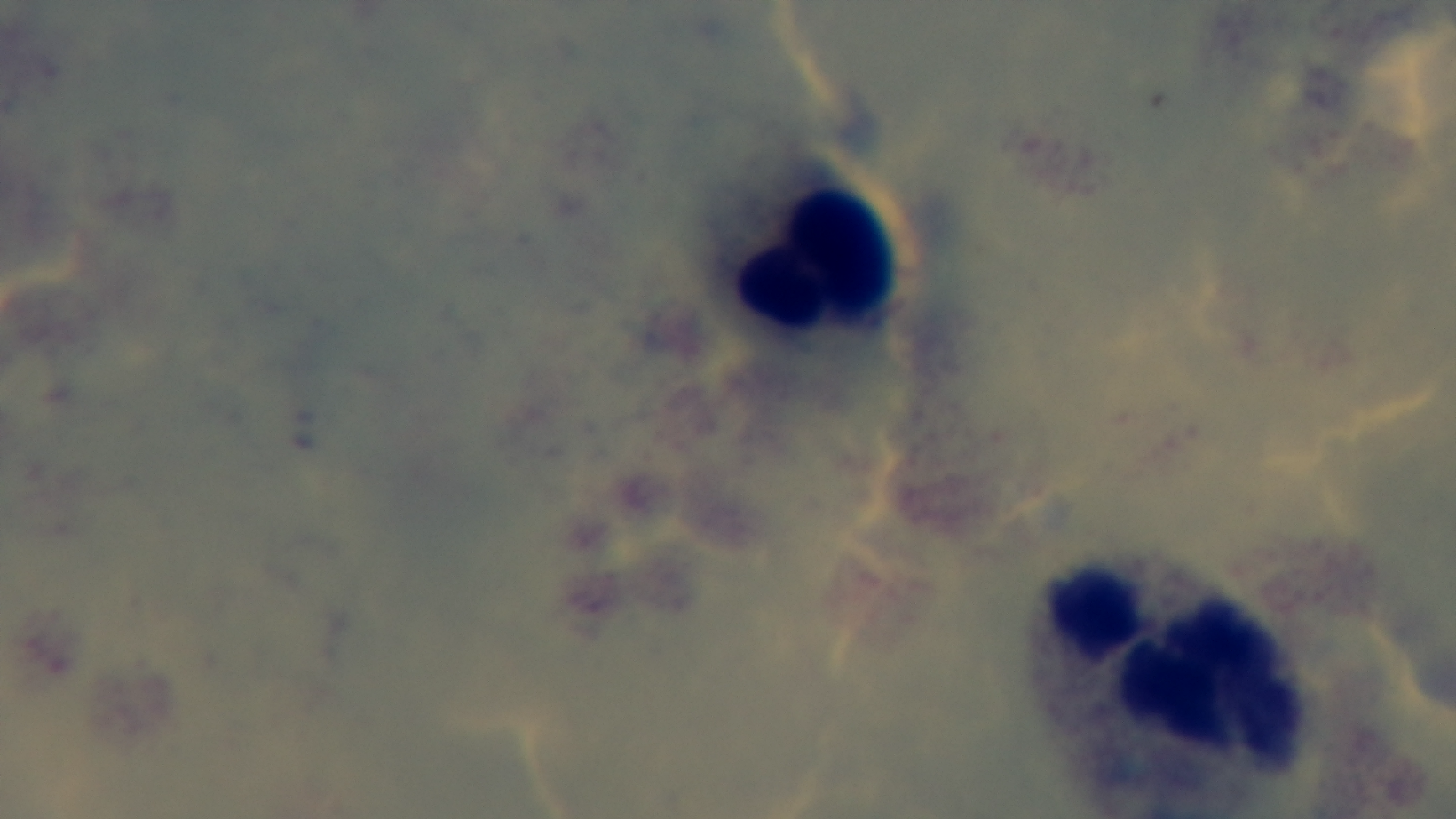

objective = 100x oil immersion
preparation = thick blood film
modality = light microscopy
field of view = one from the slide
malaria status = uninfected
capture = mounted 4K digital camera
stain = Giemsa